Name the parasite shown.
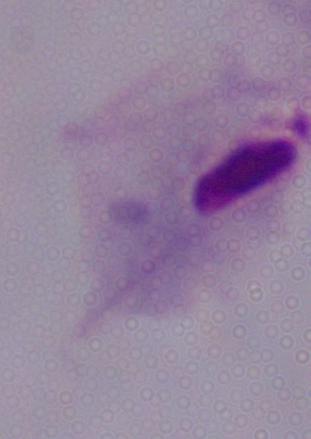
A trichomonad.

Summary:
  - Modality: micrograph
  - Magnification: 1000x